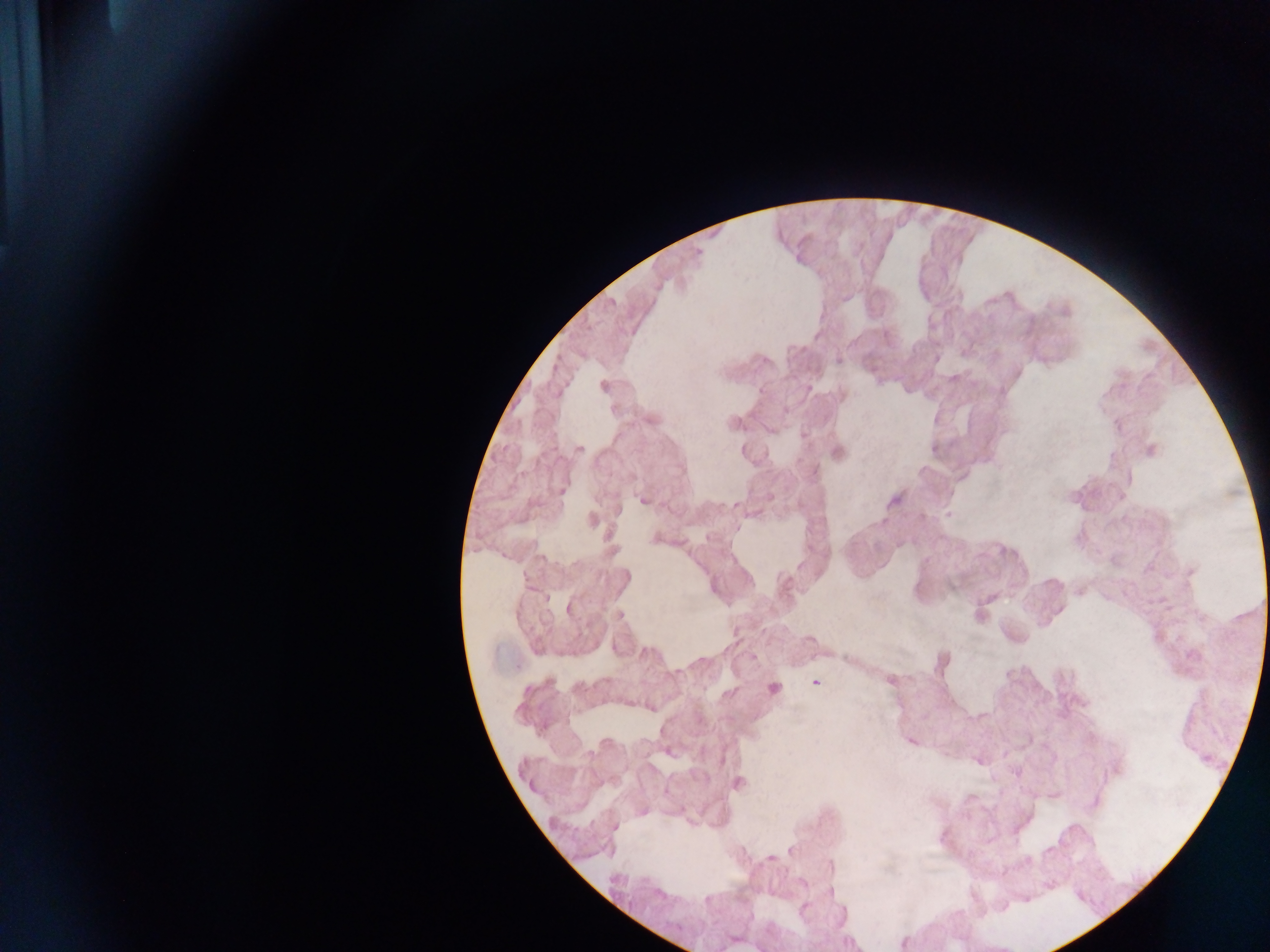

{
  "plasmodium_parasite_locations": "approximate centers as (x, y) in pixels: (761, 390), (579, 449), (643, 501), (734, 504), (800, 565), (891, 680), (815, 683), (774, 688)",
  "country": "Ghana",
  "field_of_view": "single",
  "capture": "mobile-phone photograph through a microscope",
  "preparation": "thick blood film",
  "image_size": "1270×952 pixels"
}